Give the extent of all Plasmodium falciparum-infected red blood cells.
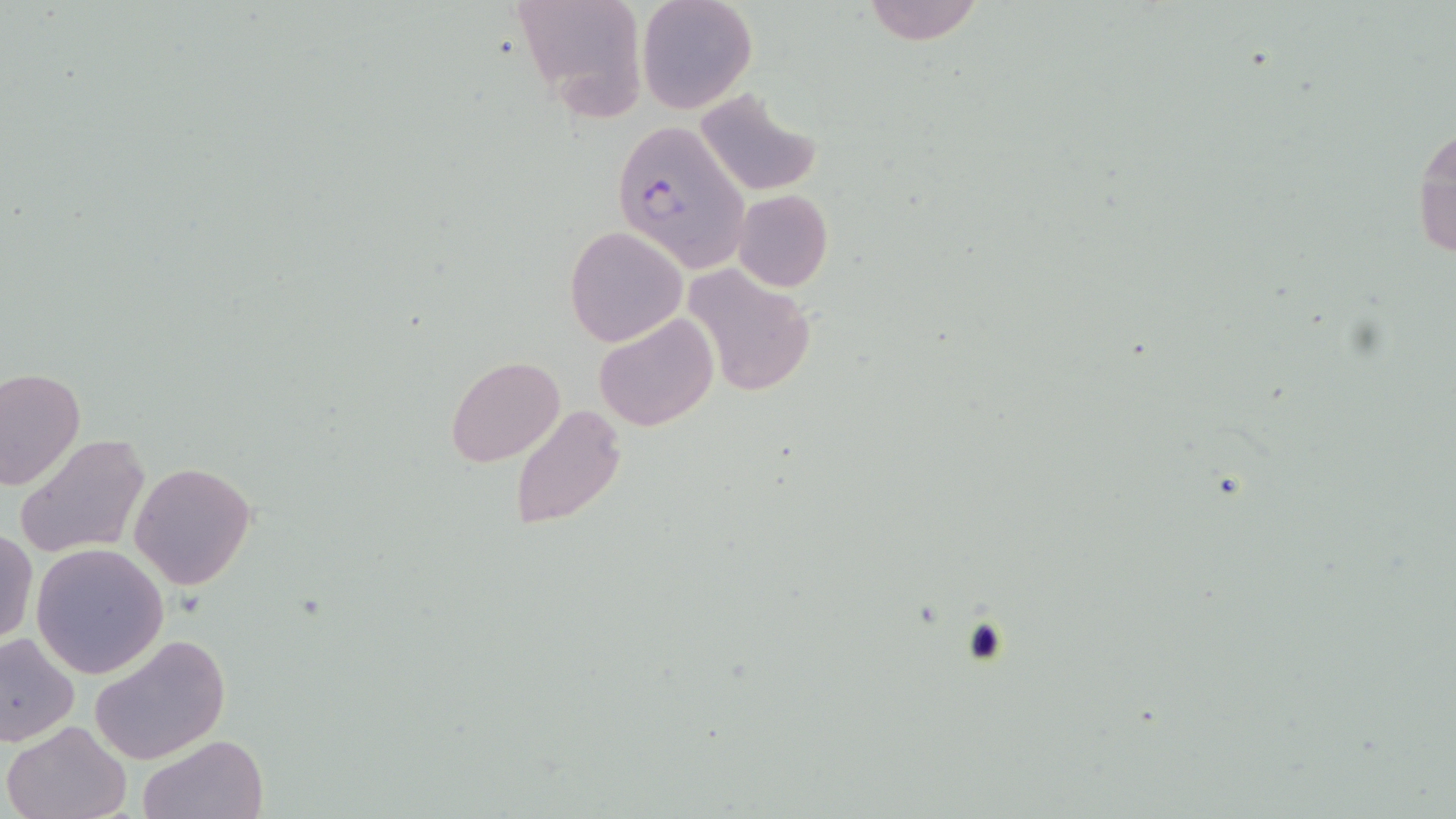

Approximate bounding boxes as named x1/y1/x2/y2 corners in pixels.
Plasmodium falciparum-infected red blood cells: (x1=611, y1=120, x2=750, y2=273).

slide-level diagnosis = Plasmodium falciparum
uninfected red blood cell locations = approximate bounding boxes as named x1/y1/x2/y2 corners in pixels: (x1=507, y1=0, x2=649, y2=122), (x1=638, y1=0, x2=757, y2=115), (x1=862, y1=0, x2=985, y2=45), (x1=693, y1=89, x2=821, y2=197), (x1=1411, y1=119, x2=1456, y2=265), (x1=733, y1=189, x2=833, y2=293), (x1=565, y1=226, x2=686, y2=346), (x1=684, y1=265, x2=816, y2=398), (x1=595, y1=312, x2=717, y2=432), (x1=446, y1=357, x2=564, y2=466), (x1=0, y1=367, x2=85, y2=492), (x1=511, y1=405, x2=627, y2=528), (x1=13, y1=432, x2=152, y2=559), (x1=129, y1=461, x2=257, y2=590), (x1=1, y1=526, x2=37, y2=647), (x1=30, y1=544, x2=169, y2=679), (x1=0, y1=630, x2=80, y2=746), (x1=89, y1=634, x2=231, y2=764), (x1=3, y1=720, x2=132, y2=818), (x1=141, y1=733, x2=267, y2=819)
modality = optical microscopy
image size = 1456×819 pixels
platelet locations = approximate bounding boxes as named x1/y1/x2/y2 corners in pixels: (x1=960, y1=616, x2=1014, y2=666)
magnification = 1000x
stain = May-Grünwald-Giemsa
preparation = thin blood film
field of view = one of a larger specimen